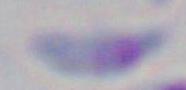
Micrograph. Captured at 1000x magnification. Toxoplasma gondii is seen.